Point out each Plasmodium parasite.
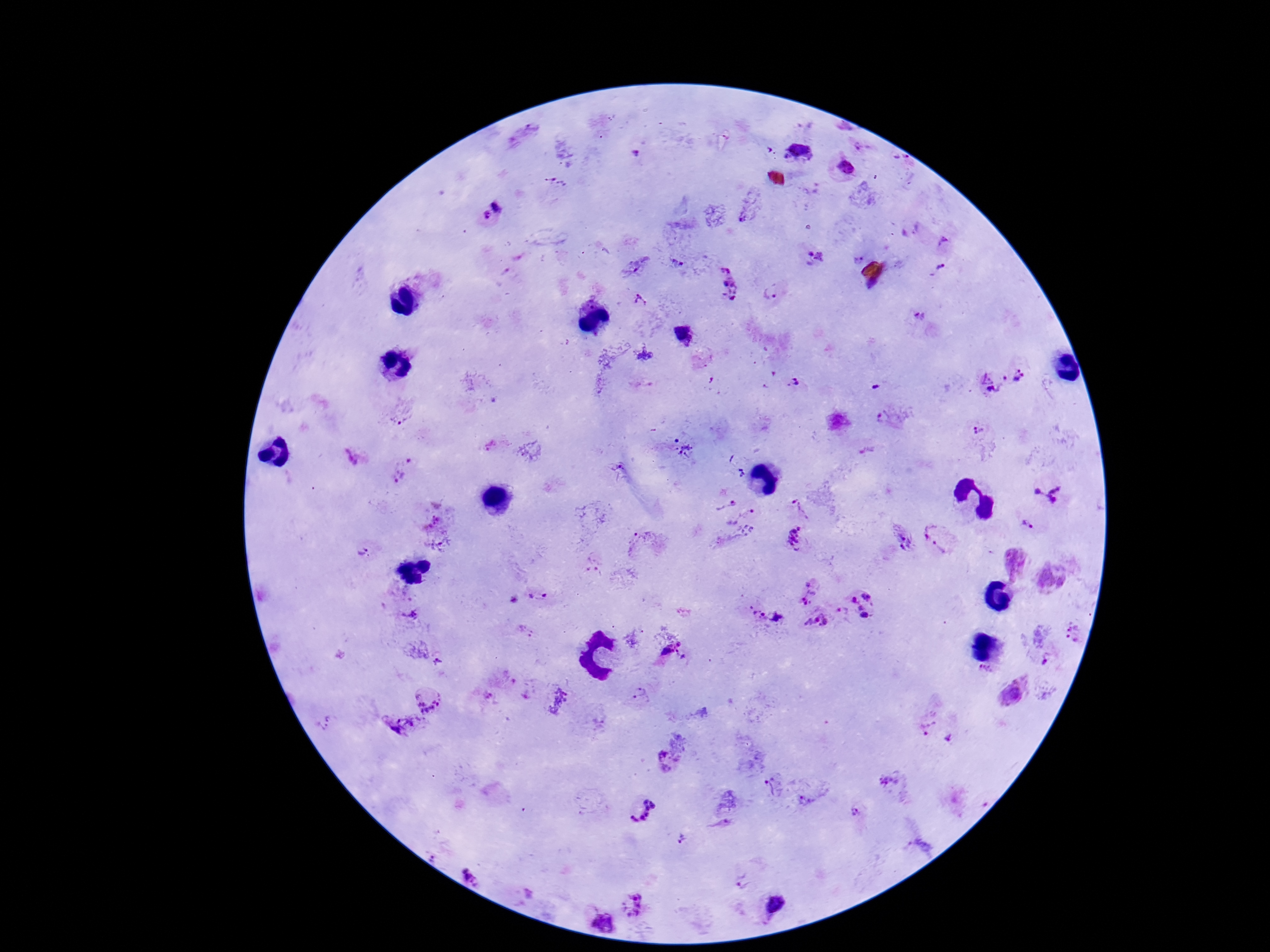
Approximate object centers, in pixels from the top-left corner.
Plasmodium parasites: (x=864, y=149), (x=797, y=151), (x=635, y=154), (x=901, y=161), (x=843, y=169), (x=557, y=184), (x=498, y=205), (x=484, y=217), (x=945, y=243), (x=816, y=259), (x=857, y=259), (x=677, y=264), (x=941, y=270), (x=722, y=282), (x=771, y=291), (x=641, y=300), (x=921, y=318), (x=644, y=355), (x=1020, y=376), (x=993, y=383), (x=798, y=384), (x=401, y=411), (x=888, y=418), (x=979, y=431), (x=685, y=450), (x=357, y=455), (x=404, y=469), (x=1050, y=490), (x=721, y=494), (x=799, y=509), (x=430, y=517), (x=745, y=520), (x=1029, y=525), (x=944, y=534), (x=796, y=543), (x=901, y=543), (x=646, y=544), (x=363, y=550), (x=446, y=552), (x=596, y=563), (x=809, y=591), (x=538, y=598), (x=514, y=600), (x=863, y=607), (x=411, y=615), (x=841, y=615), (x=765, y=618), (x=816, y=623), (x=526, y=631), (x=1075, y=635), (x=675, y=652), (x=1044, y=658), (x=437, y=661), (x=983, y=671), (x=1012, y=692), (x=428, y=695), (x=642, y=696), (x=562, y=701), (x=924, y=722), (x=399, y=731), (x=950, y=739), (x=666, y=760), (x=890, y=781), (x=775, y=786), (x=809, y=800), (x=640, y=808), (x=857, y=810), (x=721, y=824), (x=683, y=839), (x=919, y=848), (x=473, y=865), (x=740, y=882), (x=632, y=904), (x=773, y=906), (x=602, y=921).

Summary:
  - Magnification: 100x
  - Capture: smartphone camera through the microscope eyepiece
  - Preparation: thick blood smear
  - Patient malaria status: infected
  - Image size: 1270×952 pixels
  - Stain: Giemsa
  - Field of view: one from this slide